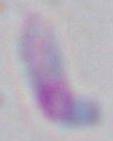

Summary:
  - Modality: photomicrograph
  - Identification: Toxoplasma gondii
  - Magnification: 1000x